Evaluate for malaria.
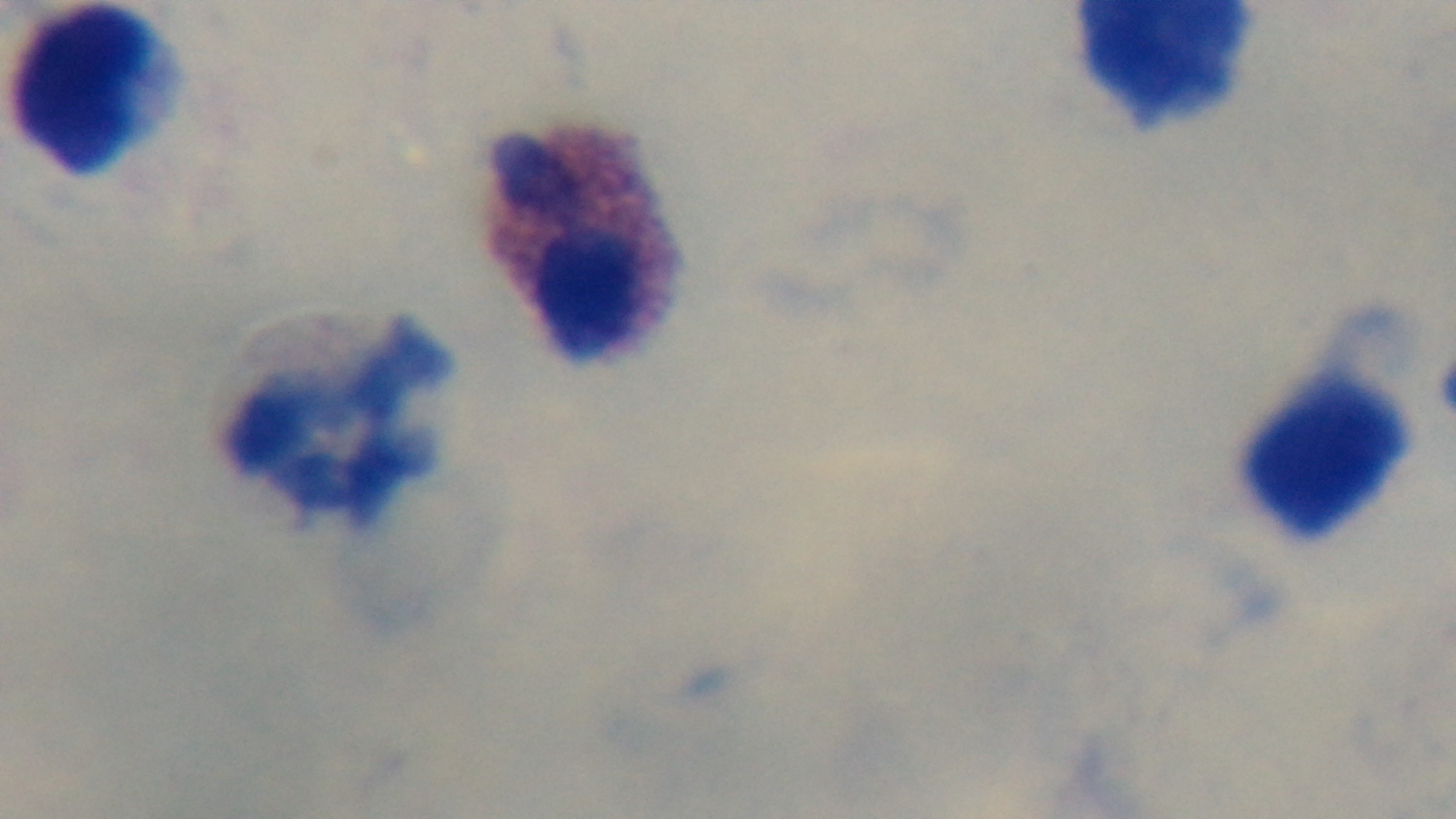

Negative.

Summary:
  - Stain: Giemsa
  - Objective: 100x oil immersion
  - Preparation: thick blood film
  - Capture: mounted 4K digital camera
  - Field of view: one from the slide
  - Modality: light microscopy